Report the malaria status of this cell.
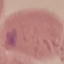
Uninfected.

Thin blood smear. Photographed with a smartphone camera at the microscope eyepiece. Automatically extracted cell patch, resized to 64 × 64 pixels. Giemsa-stained preparation.